Classify this cell by malaria status.
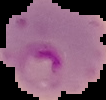

It is parasitized.

From a thin blood film. Image is 106×100 pixels. The area outside the segmented cell region is set to black.